Name the cell type shown.
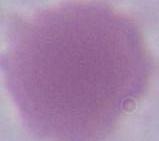
This is an erythrocyte.

Summary:
  - Modality: photomicrograph
  - Magnification: 1000x